Look for Plasmodium parasites.
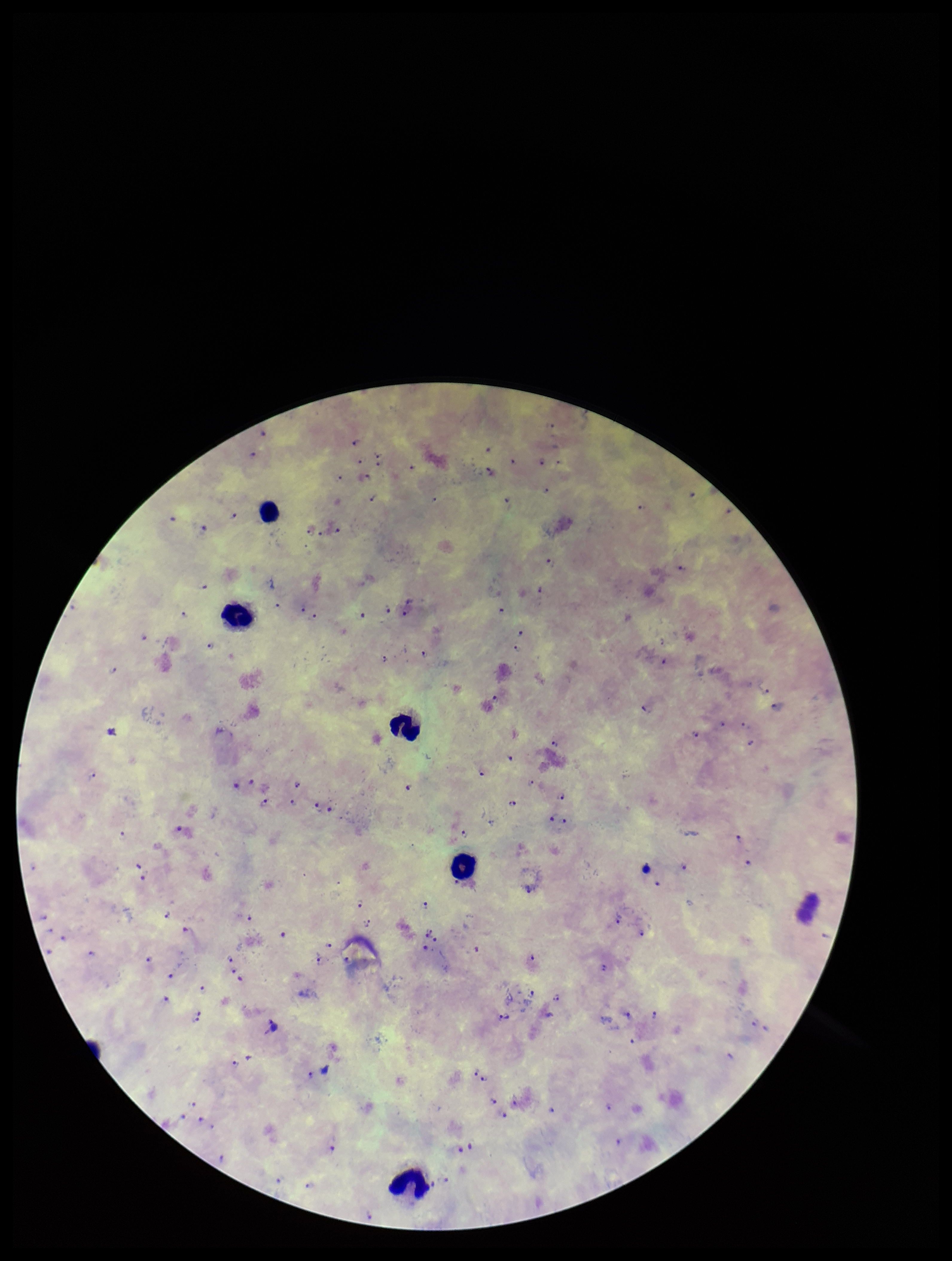

Identified.

Patient malaria status: infected. Single field of view. Image is 952×1261 pixels. Species reported for this patient: Plasmodium falciparum. Photographed through the microscope eyepiece with a smartphone camera. Leukocyte count: 5. Preparation: thick smear. Giemsa stain. Parasite count: 100.